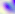
Micrograph. 400x magnification. Toxoplasma gondii is shown.